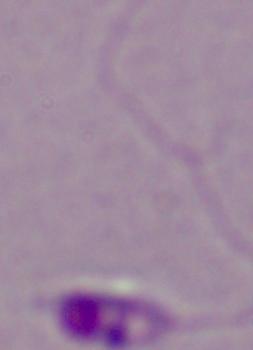
1000x magnification. Photomicrograph. A Leishmania parasite is shown.